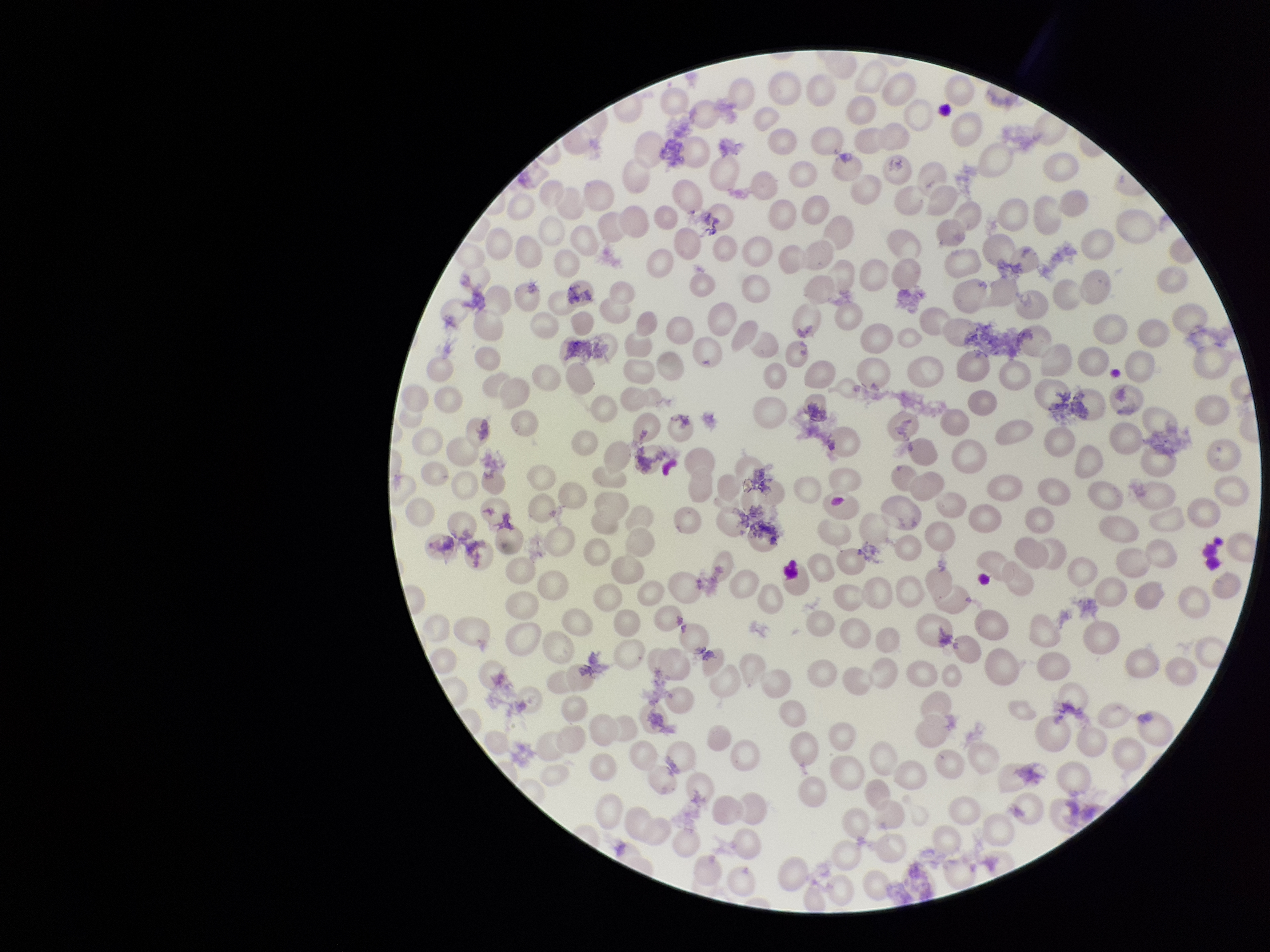 Parasitized red blood cells: none detected. Smartphone photograph taken through the eyepiece of a microscope. Parasitized red blood cell count: 0. Stained with Giemsa. One field from this slide. Image is 1270×952 pixels. Red blood cell count: 248. Preparation: thin blood smear. Patient malaria status: negative.